Assess this cell for malaria.
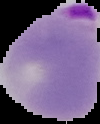

Parasitized.

{
  "image_type": "cell region segmented out of the field of view; surrounding area masked to black",
  "image_size": "100×124 pixels",
  "preparation": "thin blood smear"
}